Classify this cell by malaria status.
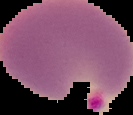

Parasitized.

image type = cell region segmented out of the field of view; surrounding area masked to black
image size = 133×115 pixels
preparation = thin blood film